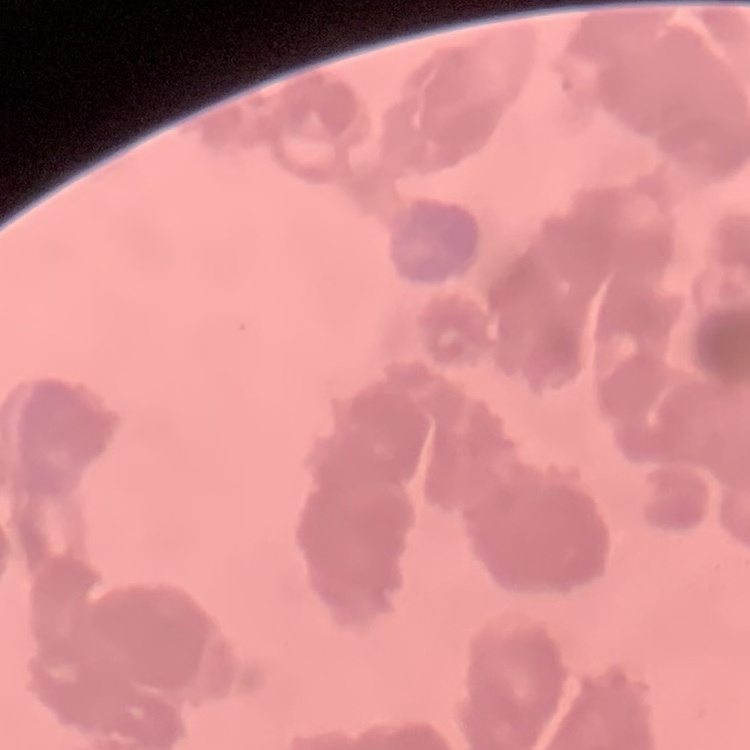

The red blood cells show rouleaux formation. Thin blood smear. Field's or Giemsa stain. One tile cut from a larger photomicrograph.